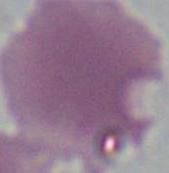

{
  "magnification": "1000x",
  "identification": "red blood cell",
  "modality": "photomicrograph"
}